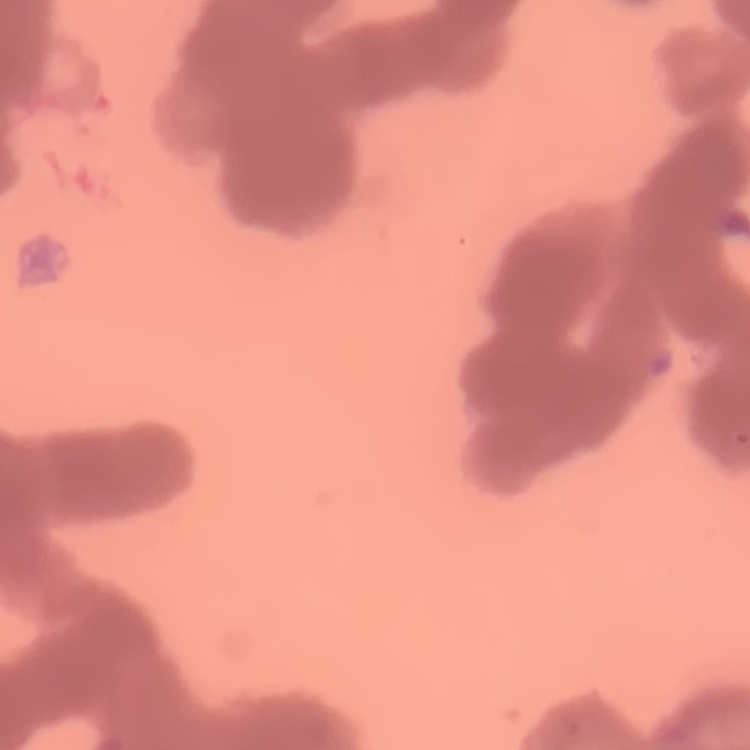
Summary:
  - Erythrocyte morphology: rouleaux formation
  - Image type: square crop of a larger photomicrograph
  - Stain: Field's or Giemsa
  - Preparation: thin peripheral smear